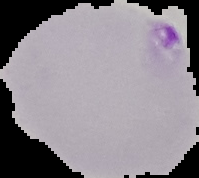

{
  "preparation": "thin blood smear",
  "image_size": "199×178 pixels",
  "malaria_status": "parasitized",
  "image_type": "cell region segmented out of the field of view; surrounding area masked to black"
}